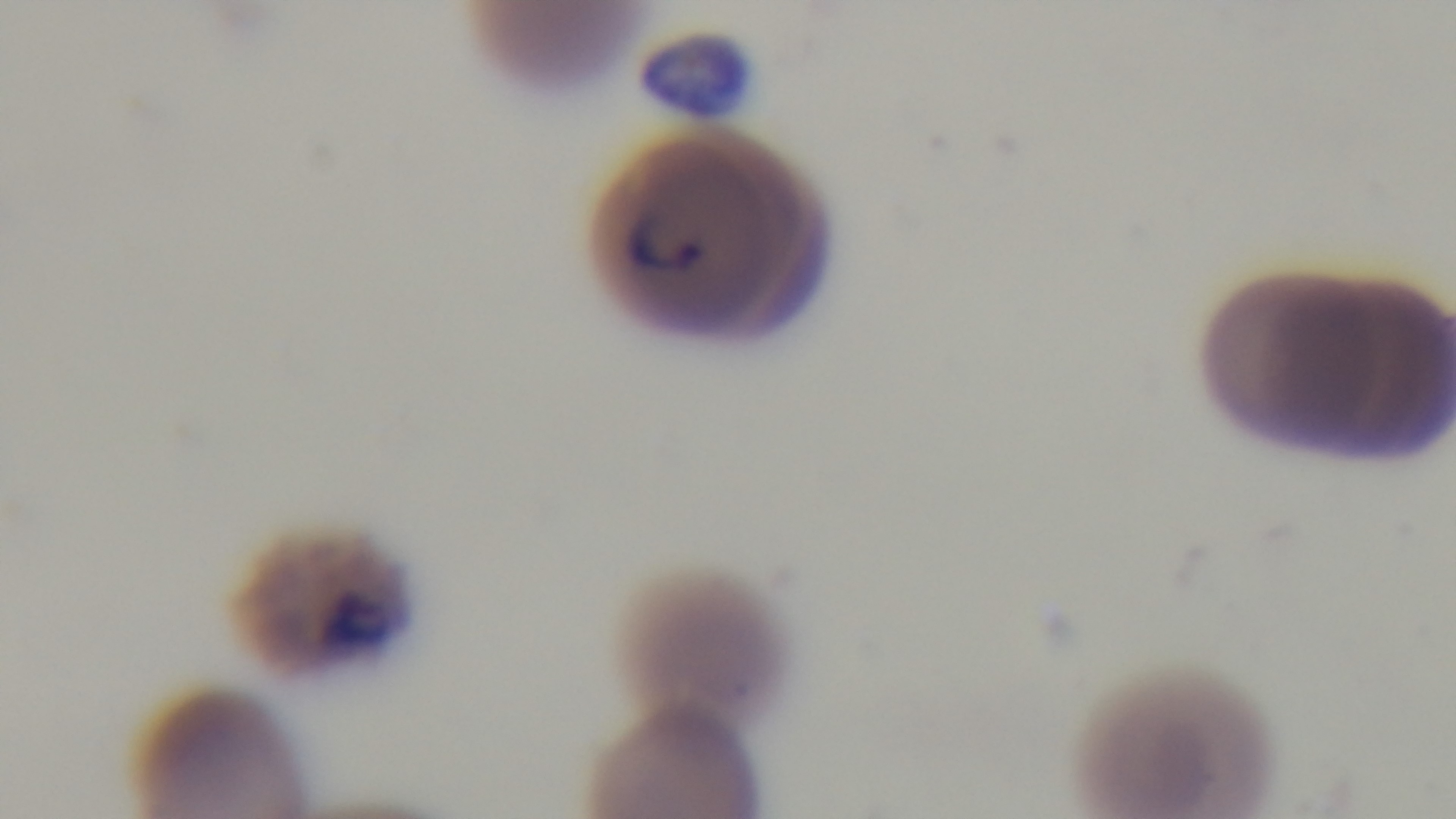 Photomicrograph. Preparation: thin blood film. Malaria status: infected. One field from the slide. Giemsa stain. Mounted 4K digital camera. 100x oil-immersion objective.